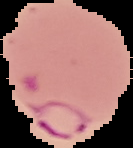

image size = 133×148 pixels
image type = cell region segmented out of the field of view; surrounding area masked to black
malaria status = parasitized
preparation = thin blood film